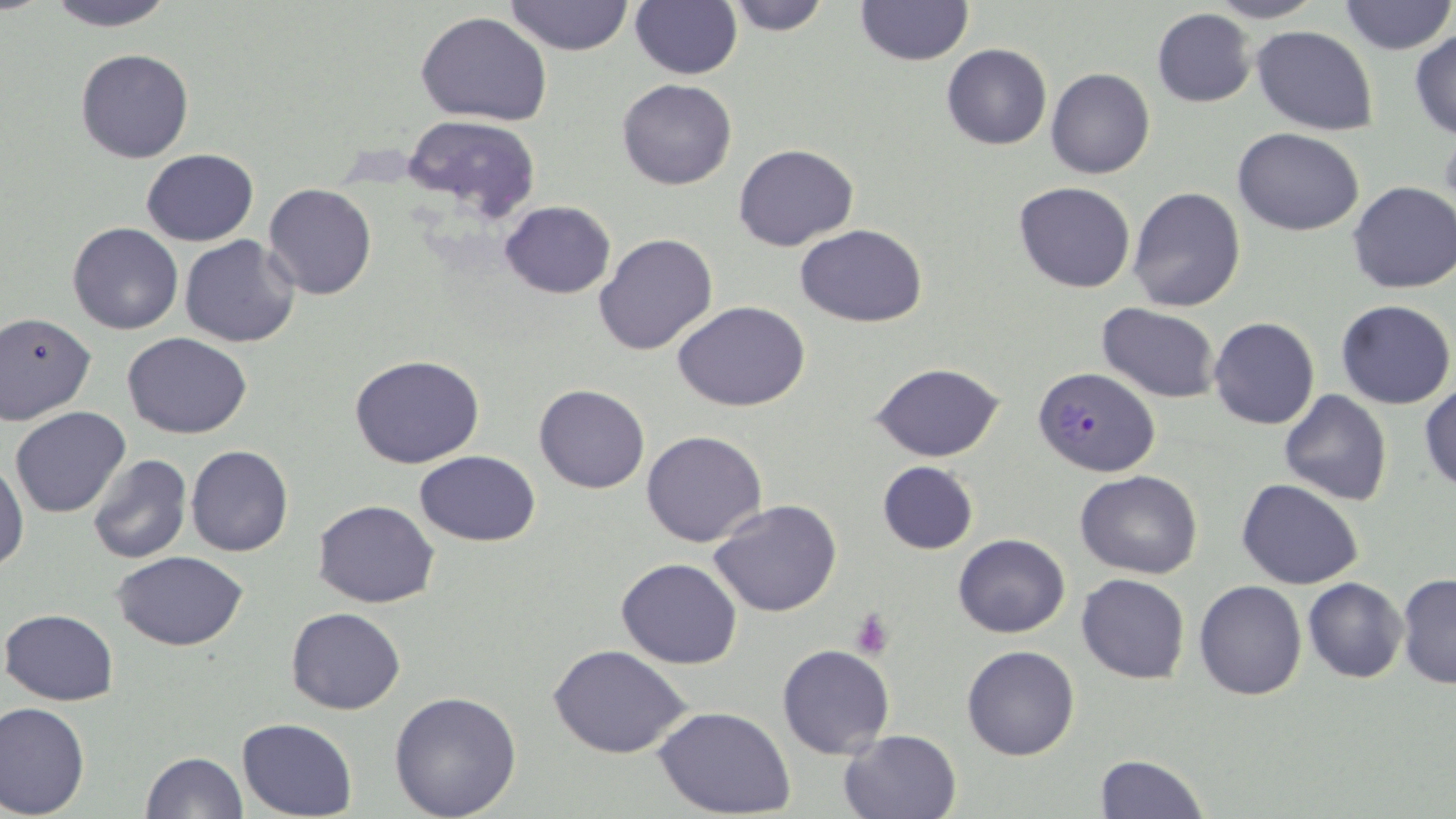

{
  "slide_level_diagnosis": "Plasmodium falciparum",
  "stain": "May-Grünwald-Giemsa",
  "modality": "optical microscopy",
  "plasmodium_falciparum_infected_red_blood_cell_locations": "approximate bounding boxes as [x1, y1, x2, y2] in pixels: [1033, 366, 1160, 479]",
  "field_of_view": "one of a larger specimen",
  "platelet_locations": "approximate bounding boxes as [x1, y1, x2, y2] in pixels: [849, 607, 896, 658]",
  "preparation": "thin blood smear",
  "uninfected_red_blood_cell_locations": "approximate bounding boxes as [x1, y1, x2, y2] in pixels: [45, 0, 176, 31], [505, 0, 633, 55], [629, 0, 741, 80], [723, 0, 835, 35], [853, 0, 975, 66], [1203, 0, 1328, 24], [1339, 0, 1454, 56], [1152, 9, 1257, 108], [415, 11, 554, 127], [1253, 25, 1378, 133], [1410, 28, 1456, 142], [941, 44, 1051, 150], [75, 48, 195, 163], [1046, 69, 1155, 179], [617, 79, 736, 190], [401, 115, 542, 220], [1234, 127, 1365, 237], [733, 142, 859, 251], [141, 149, 259, 246], [1348, 181, 1456, 295], [262, 182, 378, 300], [1014, 182, 1136, 293], [1127, 187, 1247, 313], [500, 201, 616, 298], [66, 222, 183, 335], [795, 223, 927, 328], [594, 233, 718, 357], [180, 235, 301, 348], [1336, 299, 1454, 409], [673, 301, 810, 412], [1097, 304, 1221, 402], [0, 313, 96, 423], [1209, 317, 1320, 431], [122, 332, 253, 439], [350, 355, 485, 468], [869, 361, 1006, 462], [1420, 382, 1456, 490], [534, 383, 649, 493], [1279, 390, 1392, 507], [9, 406, 131, 518], [641, 429, 767, 547], [185, 444, 294, 557], [415, 450, 541, 545], [0, 454, 27, 574], [88, 454, 193, 565], [877, 461, 979, 554], [1076, 470, 1202, 579], [1221, 477, 1342, 690], [1237, 478, 1363, 589], [312, 499, 439, 606], [709, 499, 843, 619], [952, 533, 1070, 638], [113, 551, 250, 651], [616, 557, 742, 669], [1077, 573, 1189, 684], [1398, 573, 1456, 689], [1303, 578, 1408, 684], [1194, 581, 1307, 700], [285, 606, 406, 716], [1, 609, 120, 706], [546, 644, 694, 759], [961, 644, 1080, 761], [779, 647, 895, 758], [389, 690, 522, 819], [1, 701, 90, 818], [654, 706, 797, 817], [237, 718, 358, 818], [840, 729, 963, 819], [141, 750, 248, 818], [1095, 755, 1210, 818]",
  "magnification": "1000x",
  "image_size": "1456×819 pixels"
}